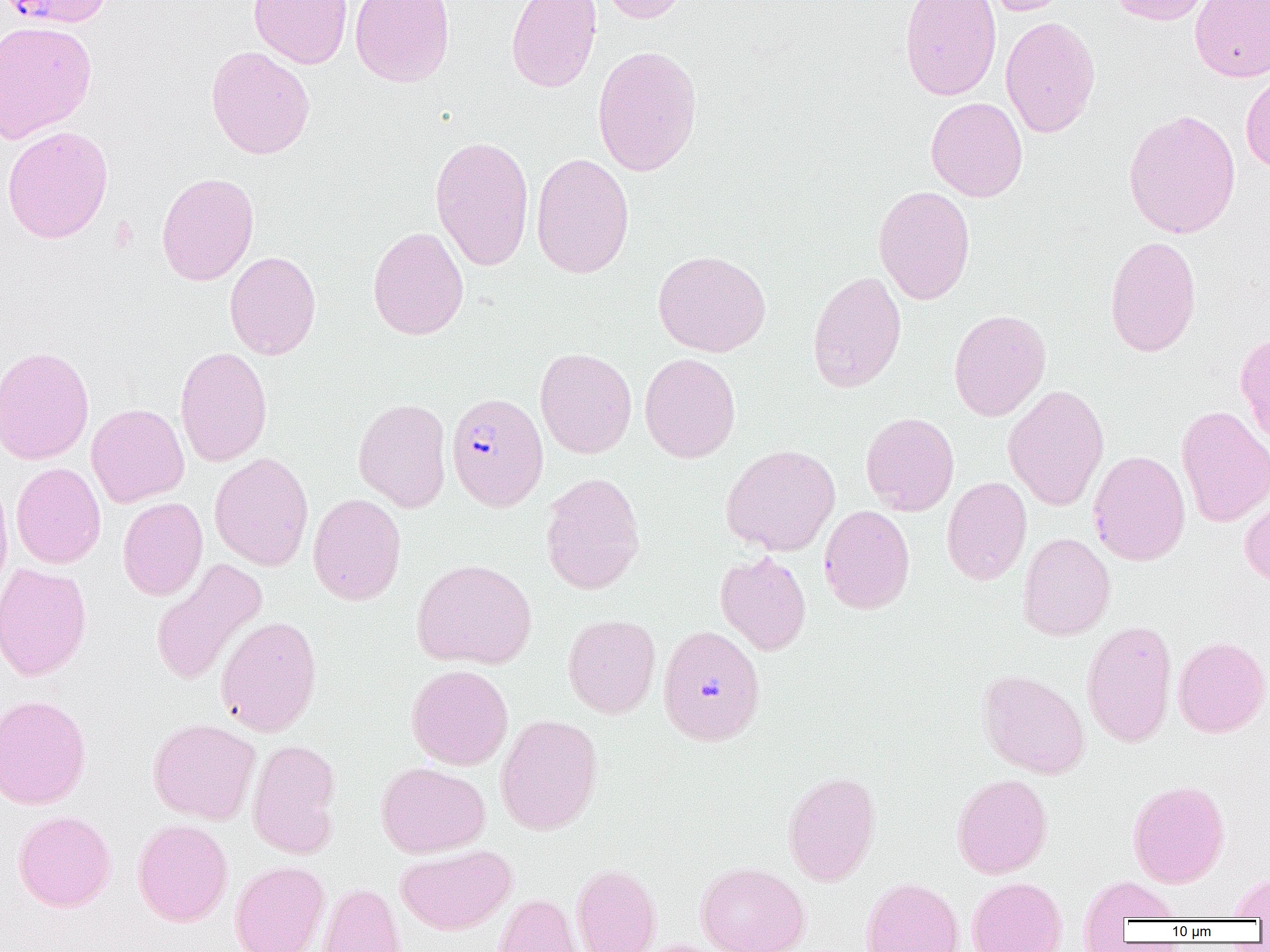

Summary:
  - Coordinate format: approximate bounding boxes as named x1/y1/x2/y2 corners in pixels
  - Uninfected red blood cell locations: (x1=249, y1=0, x2=352, y2=68), (x1=350, y1=0, x2=455, y2=88), (x1=505, y1=0, x2=602, y2=93), (x1=596, y1=0, x2=689, y2=24), (x1=899, y1=0, x2=1002, y2=101), (x1=982, y1=0, x2=1072, y2=16), (x1=1107, y1=0, x2=1212, y2=25), (x1=1189, y1=0, x2=1270, y2=82), (x1=1000, y1=15, x2=1101, y2=138), (x1=0, y1=20, x2=97, y2=143), (x1=592, y1=44, x2=702, y2=177), (x1=206, y1=46, x2=315, y2=160), (x1=1240, y1=69, x2=1270, y2=172), (x1=925, y1=97, x2=1027, y2=202), (x1=1123, y1=108, x2=1241, y2=239), (x1=1, y1=125, x2=114, y2=243), (x1=430, y1=135, x2=534, y2=271), (x1=531, y1=152, x2=635, y2=280), (x1=156, y1=172, x2=259, y2=286), (x1=873, y1=185, x2=976, y2=305), (x1=368, y1=226, x2=469, y2=341), (x1=1104, y1=235, x2=1202, y2=358), (x1=652, y1=249, x2=771, y2=357), (x1=225, y1=251, x2=321, y2=360), (x1=807, y1=270, x2=907, y2=393), (x1=948, y1=308, x2=1051, y2=421), (x1=1235, y1=332, x2=1270, y2=446), (x1=0, y1=346, x2=95, y2=465), (x1=175, y1=346, x2=273, y2=467), (x1=535, y1=347, x2=637, y2=458), (x1=639, y1=352, x2=741, y2=464), (x1=1003, y1=385, x2=1109, y2=511), (x1=353, y1=397, x2=452, y2=512), (x1=86, y1=403, x2=189, y2=507), (x1=1175, y1=405, x2=1270, y2=527), (x1=861, y1=412, x2=960, y2=516), (x1=721, y1=443, x2=841, y2=556), (x1=1088, y1=450, x2=1191, y2=566), (x1=209, y1=452, x2=313, y2=571), (x1=11, y1=462, x2=105, y2=569), (x1=540, y1=472, x2=646, y2=595), (x1=0, y1=476, x2=13, y2=598), (x1=941, y1=476, x2=1032, y2=585), (x1=1240, y1=489, x2=1270, y2=587), (x1=308, y1=493, x2=406, y2=605), (x1=118, y1=497, x2=208, y2=601), (x1=819, y1=505, x2=915, y2=614), (x1=1018, y1=532, x2=1115, y2=641), (x1=715, y1=551, x2=812, y2=655), (x1=411, y1=558, x2=537, y2=670), (x1=151, y1=559, x2=267, y2=686), (x1=0, y1=563, x2=92, y2=681), (x1=562, y1=614, x2=661, y2=719), (x1=216, y1=615, x2=321, y2=737), (x1=1081, y1=620, x2=1177, y2=748), (x1=657, y1=624, x2=766, y2=746), (x1=1172, y1=635, x2=1270, y2=738), (x1=406, y1=664, x2=513, y2=770), (x1=977, y1=668, x2=1090, y2=779), (x1=0, y1=694, x2=91, y2=810), (x1=495, y1=713, x2=603, y2=835), (x1=147, y1=718, x2=261, y2=824), (x1=247, y1=739, x2=341, y2=858), (x1=376, y1=761, x2=490, y2=858), (x1=783, y1=770, x2=881, y2=887), (x1=951, y1=773, x2=1053, y2=879), (x1=1128, y1=779, x2=1230, y2=888), (x1=13, y1=810, x2=116, y2=912), (x1=132, y1=819, x2=233, y2=926), (x1=395, y1=844, x2=517, y2=935), (x1=229, y1=860, x2=329, y2=952), (x1=696, y1=861, x2=810, y2=952), (x1=571, y1=863, x2=661, y2=952), (x1=1228, y1=872, x2=1270, y2=919), (x1=1077, y1=875, x2=1182, y2=931), (x1=861, y1=876, x2=963, y2=952), (x1=967, y1=876, x2=1067, y2=952), (x1=317, y1=882, x2=406, y2=952), (x1=493, y1=893, x2=582, y2=952), (x1=630, y1=939, x2=731, y2=952)
  - Plasmodium falciparum-infected red blood cell locations: (x1=3, y1=0, x2=112, y2=28), (x1=446, y1=392, x2=548, y2=511)
  - Slide-level diagnosis: Plasmodium falciparum
  - Field of view: one of a larger specimen
  - Modality: optical microscopy
  - Magnification: 1000x
  - Image size: 1270×952 pixels
  - Preparation: thin blood film